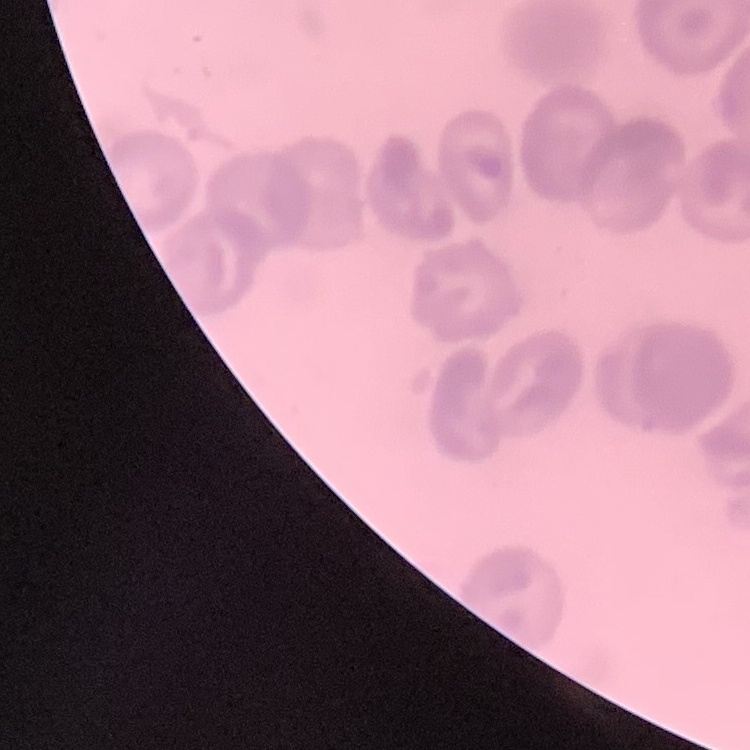
red blood cell morphology = no rouleaux formation
image type = square crop of a larger photomicrograph
preparation = thin peripheral smear
stain = Field's or Giemsa